Name the parasite shown.
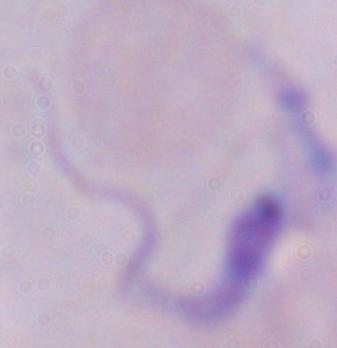
This is a trypanosome.

modality = micrograph
magnification = 1000x